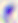 Photomicrograph. 400x magnification. Toxoplasma gondii is shown.